Locate and identify every blood parasite.
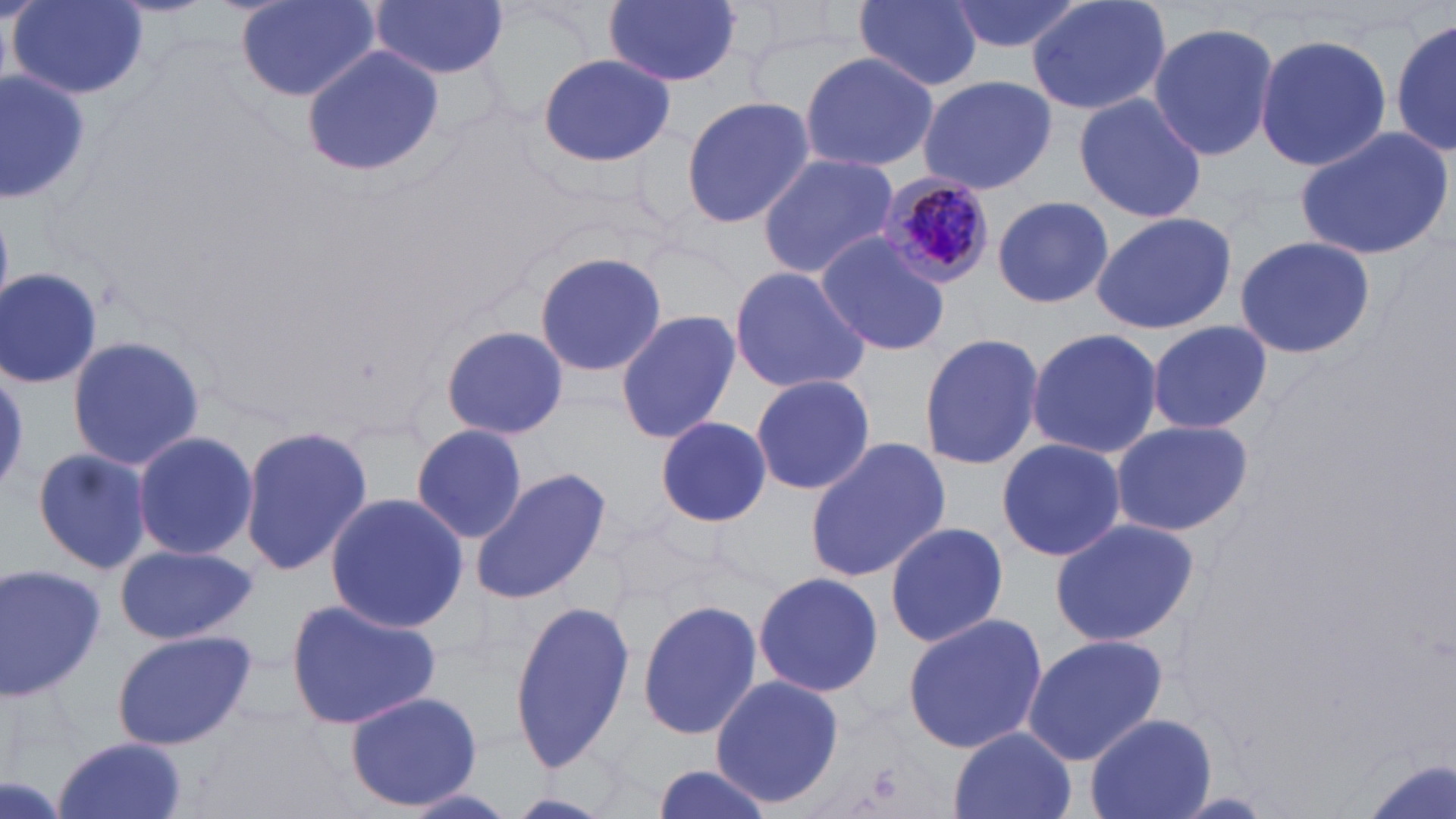

Approximate bounding boxes as named x1/y1/x2/y2 corners in pixels.
Plasmodium malariae-infected red blood cells: (x1=877, y1=171, x2=997, y2=289).
No Plasmodium falciparum, Plasmodium ovale, Plasmodium vivax, Babesia divergens, or Trypanosoma brucei observed.

slide-level diagnosis = Plasmodium malariae
uninfected red blood cell locations = approximate bounding boxes as named x1/y1/x2/y2 corners in pixels: (x1=9, y1=0, x2=149, y2=100), (x1=234, y1=0, x2=381, y2=101), (x1=370, y1=0, x2=509, y2=80), (x1=602, y1=0, x2=741, y2=87), (x1=853, y1=0, x2=983, y2=90), (x1=946, y1=0, x2=1088, y2=56), (x1=1025, y1=0, x2=1172, y2=118), (x1=1390, y1=13, x2=1455, y2=161), (x1=1147, y1=20, x2=1281, y2=163), (x1=1253, y1=34, x2=1391, y2=174), (x1=300, y1=47, x2=444, y2=177), (x1=797, y1=50, x2=939, y2=172), (x1=537, y1=53, x2=676, y2=168), (x1=0, y1=69, x2=91, y2=197), (x1=916, y1=75, x2=1057, y2=194), (x1=1071, y1=91, x2=1206, y2=224), (x1=681, y1=95, x2=817, y2=230), (x1=1294, y1=125, x2=1454, y2=264), (x1=756, y1=152, x2=900, y2=279), (x1=991, y1=194, x2=1114, y2=308), (x1=1091, y1=210, x2=1240, y2=336), (x1=814, y1=233, x2=952, y2=355), (x1=1232, y1=234, x2=1375, y2=358), (x1=532, y1=249, x2=665, y2=381), (x1=728, y1=264, x2=873, y2=392), (x1=1, y1=266, x2=106, y2=388), (x1=615, y1=309, x2=741, y2=446), (x1=1146, y1=318, x2=1273, y2=434), (x1=443, y1=324, x2=569, y2=441), (x1=1025, y1=327, x2=1164, y2=460), (x1=918, y1=332, x2=1046, y2=471), (x1=65, y1=336, x2=206, y2=471), (x1=750, y1=373, x2=876, y2=496), (x1=655, y1=416, x2=771, y2=528), (x1=1110, y1=420, x2=1252, y2=535), (x1=237, y1=423, x2=371, y2=580), (x1=410, y1=423, x2=528, y2=544), (x1=130, y1=428, x2=258, y2=562), (x1=995, y1=437, x2=1127, y2=563), (x1=805, y1=438, x2=952, y2=583), (x1=31, y1=446, x2=153, y2=576), (x1=470, y1=466, x2=612, y2=604), (x1=324, y1=491, x2=469, y2=631), (x1=1047, y1=517, x2=1199, y2=648), (x1=883, y1=522, x2=1010, y2=648), (x1=114, y1=545, x2=258, y2=644), (x1=0, y1=561, x2=104, y2=702), (x1=752, y1=571, x2=883, y2=697), (x1=284, y1=596, x2=444, y2=731), (x1=509, y1=597, x2=638, y2=772), (x1=637, y1=598, x2=763, y2=741), (x1=901, y1=611, x2=1048, y2=756), (x1=111, y1=630, x2=256, y2=750), (x1=1021, y1=634, x2=1169, y2=765), (x1=709, y1=672, x2=845, y2=810), (x1=344, y1=691, x2=482, y2=808), (x1=1084, y1=713, x2=1215, y2=819), (x1=947, y1=728, x2=1077, y2=819), (x1=50, y1=736, x2=192, y2=819), (x1=644, y1=764, x2=778, y2=819)
field of view = single
modality = light microscopy
preparation = thin blood smear
magnification = 1000x
image size = 1456×819 pixels
stain = May-Grünwald-Giemsa